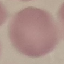
Malaria status: uninfected. Giemsa-stained preparation. Thin smear of blood. Automatically extracted cell patch, resized to 64 × 64 pixels. Acquired by smartphone through the microscope eyepiece.